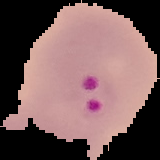

Summary:
  - Malaria status: parasitized
  - Image type: cell region segmented out of the field of view; surrounding area masked to black
  - Image size: 160×160 pixels
  - Preparation: thin blood smear